Classify this cell by malaria status.
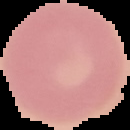

Uninfected.

image type = cell region segmented out of the field of view; surrounding area masked to black
preparation = thin blood smear
image size = 130×130 pixels